Locate every Plasmodium parasite.
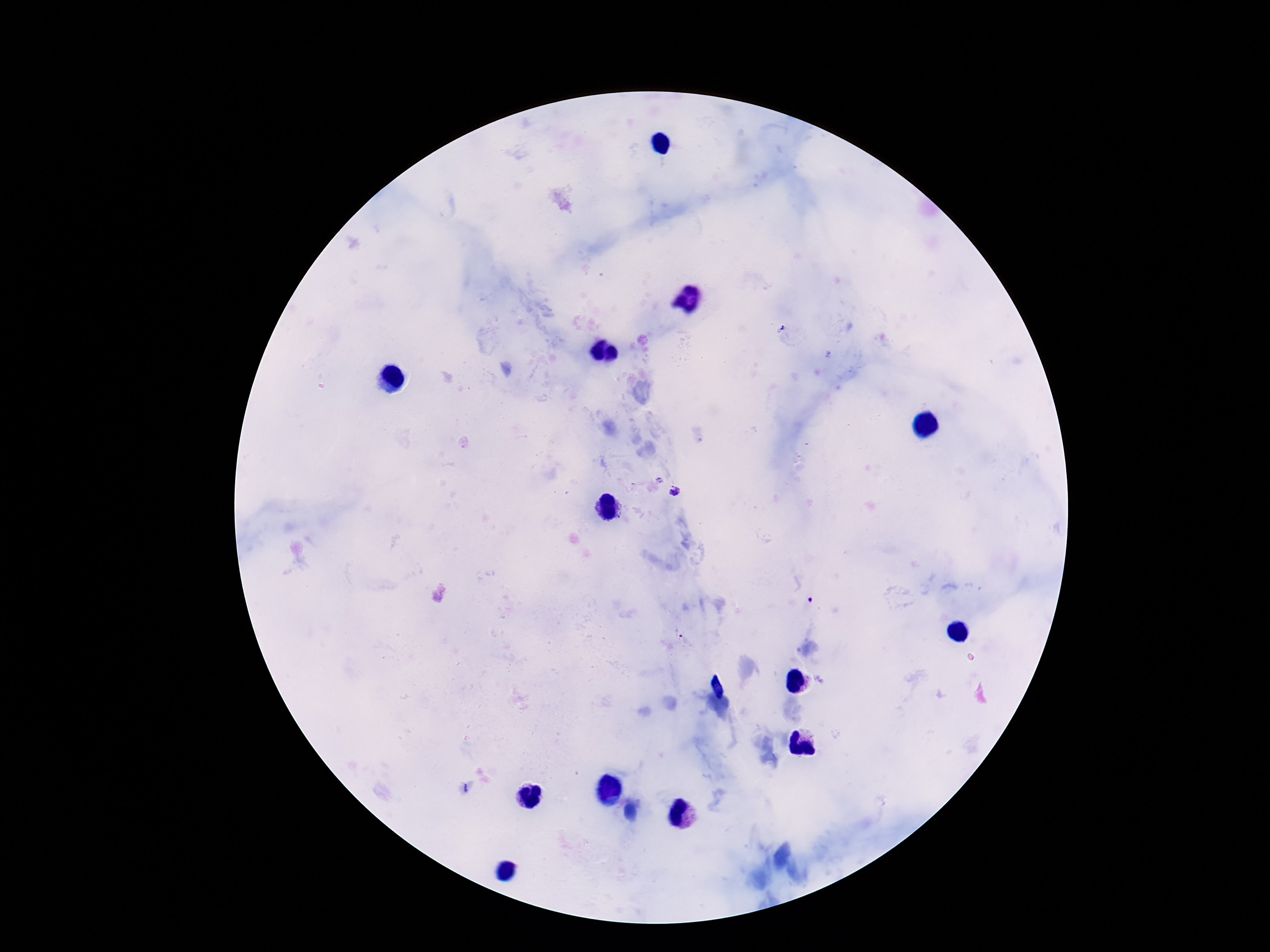
Approximate object centers, in pixels from the top-left corner.
Plasmodium parasites: (x=675, y=492), (x=678, y=631).

Summary:
  - Magnification: 100x
  - Stain: Giemsa
  - Field of view: single
  - Preparation: thick peripheral-blood smear
  - Patient malaria status: infected
  - Image size: 1270×952 pixels
  - Capture: smartphone camera through the microscope eyepiece